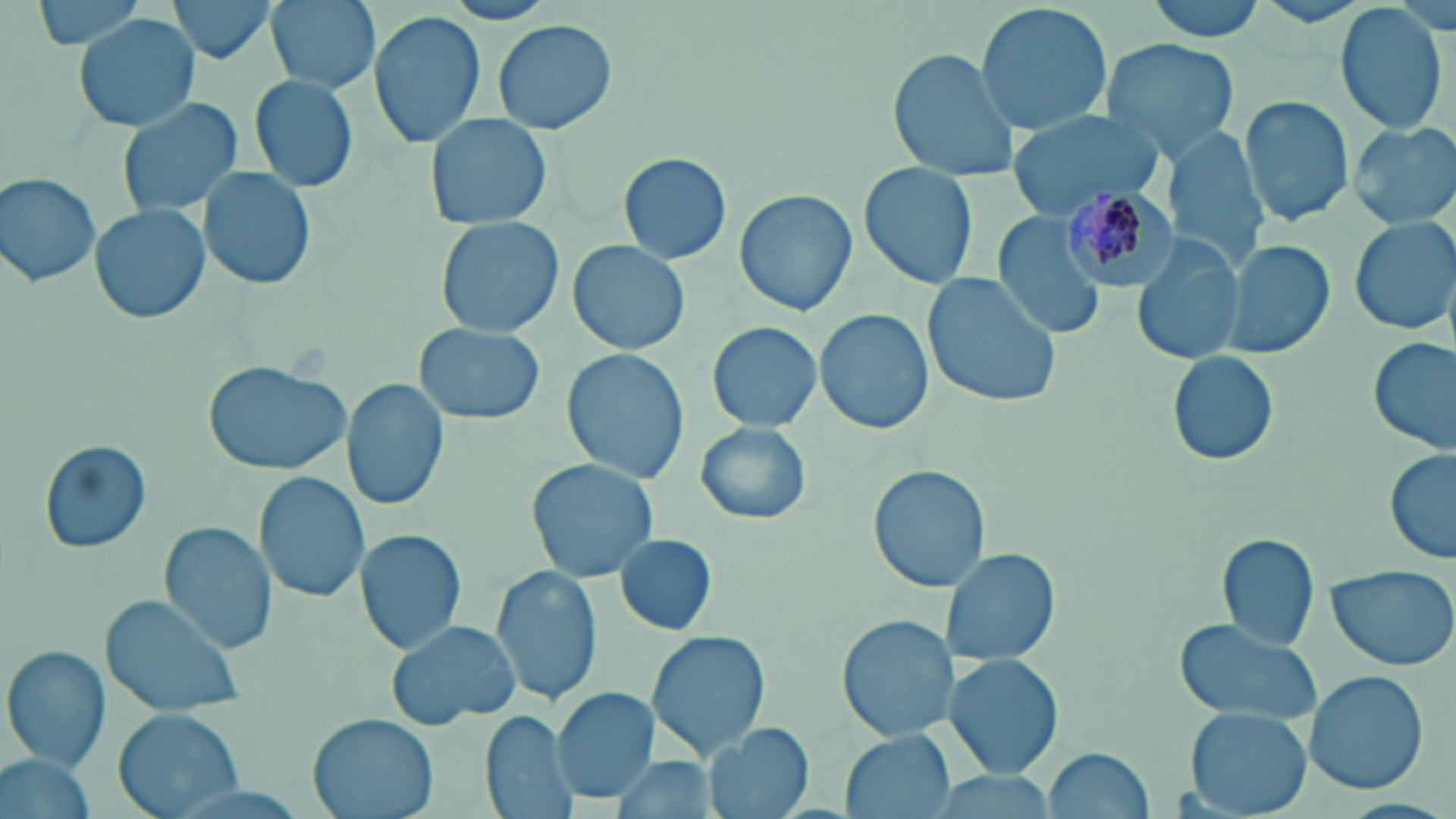

Approximate bounding boxes as named x1/y1/x2/y2 corners in pixels. Plasmodium malariae-infected red blood cell locations: (x1=1061, y1=186, x2=1182, y2=289). Uninfected red blood cell locations: (x1=24, y1=0, x2=160, y2=54), (x1=166, y1=0, x2=282, y2=66), (x1=264, y1=0, x2=379, y2=93), (x1=1145, y1=0, x2=1272, y2=42), (x1=974, y1=2, x2=1114, y2=138), (x1=1336, y1=4, x2=1450, y2=135), (x1=368, y1=9, x2=486, y2=148), (x1=73, y1=11, x2=203, y2=134), (x1=493, y1=19, x2=618, y2=135), (x1=1099, y1=38, x2=1246, y2=161), (x1=886, y1=48, x2=1022, y2=180), (x1=248, y1=73, x2=360, y2=194), (x1=117, y1=97, x2=246, y2=221), (x1=1241, y1=97, x2=1355, y2=225), (x1=1006, y1=110, x2=1171, y2=217), (x1=424, y1=113, x2=551, y2=231), (x1=1348, y1=120, x2=1456, y2=229), (x1=1165, y1=129, x2=1273, y2=269), (x1=618, y1=151, x2=732, y2=266), (x1=858, y1=162, x2=978, y2=289), (x1=202, y1=167, x2=316, y2=290), (x1=2, y1=173, x2=103, y2=289), (x1=734, y1=188, x2=857, y2=318), (x1=89, y1=205, x2=212, y2=326), (x1=989, y1=208, x2=1110, y2=338), (x1=1350, y1=214, x2=1455, y2=337), (x1=437, y1=215, x2=562, y2=337), (x1=1132, y1=234, x2=1245, y2=366), (x1=1221, y1=238, x2=1334, y2=361), (x1=567, y1=239, x2=691, y2=357), (x1=923, y1=271, x2=1065, y2=409), (x1=814, y1=309, x2=933, y2=435), (x1=704, y1=322, x2=823, y2=432), (x1=413, y1=324, x2=547, y2=425), (x1=1370, y1=335, x2=1455, y2=456), (x1=561, y1=350, x2=690, y2=483), (x1=1168, y1=351, x2=1280, y2=466), (x1=203, y1=360, x2=352, y2=474), (x1=342, y1=379, x2=448, y2=512), (x1=695, y1=421, x2=813, y2=526), (x1=40, y1=438, x2=152, y2=555), (x1=1385, y1=451, x2=1455, y2=566), (x1=525, y1=458, x2=658, y2=581), (x1=868, y1=465, x2=990, y2=592), (x1=255, y1=470, x2=370, y2=605), (x1=159, y1=522, x2=277, y2=654), (x1=355, y1=529, x2=467, y2=656), (x1=613, y1=532, x2=719, y2=635), (x1=1217, y1=534, x2=1319, y2=653), (x1=939, y1=545, x2=1059, y2=667), (x1=490, y1=563, x2=600, y2=708), (x1=1327, y1=565, x2=1456, y2=671), (x1=101, y1=593, x2=246, y2=718), (x1=837, y1=614, x2=960, y2=743), (x1=1170, y1=617, x2=1324, y2=723), (x1=386, y1=619, x2=521, y2=729), (x1=646, y1=630, x2=770, y2=762), (x1=4, y1=647, x2=111, y2=773), (x1=943, y1=651, x2=1065, y2=781), (x1=1302, y1=670, x2=1429, y2=797), (x1=553, y1=688, x2=658, y2=803), (x1=115, y1=706, x2=242, y2=818), (x1=1185, y1=707, x2=1313, y2=819), (x1=481, y1=710, x2=575, y2=819), (x1=309, y1=713, x2=439, y2=819), (x1=704, y1=722, x2=812, y2=819), (x1=842, y1=730, x2=955, y2=818), (x1=1043, y1=747, x2=1153, y2=816), (x1=3, y1=750, x2=99, y2=819), (x1=610, y1=759, x2=722, y2=816). Slide-level diagnosis: Plasmodium malariae. 1000x magnification. Thin blood film. Light microscopy. May-Grünwald-Giemsa-stained preparation. Image is 1456×819 pixels. One field of a larger specimen.